Name the parasite shown.
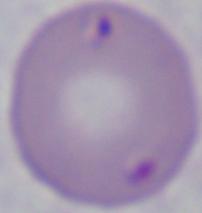

This is Babesia.

Summary:
  - Magnification: 1000x
  - Modality: micrograph